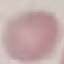
Summary:
  - Result: no malaria parasites seen
  - Stain: Giemsa
  - Preparation: thin blood film
  - Capture: smartphone through the microscope eyepiece
  - Image type: cell patch, automatically extracted from a larger field of view and resized to 64 × 64 pixels